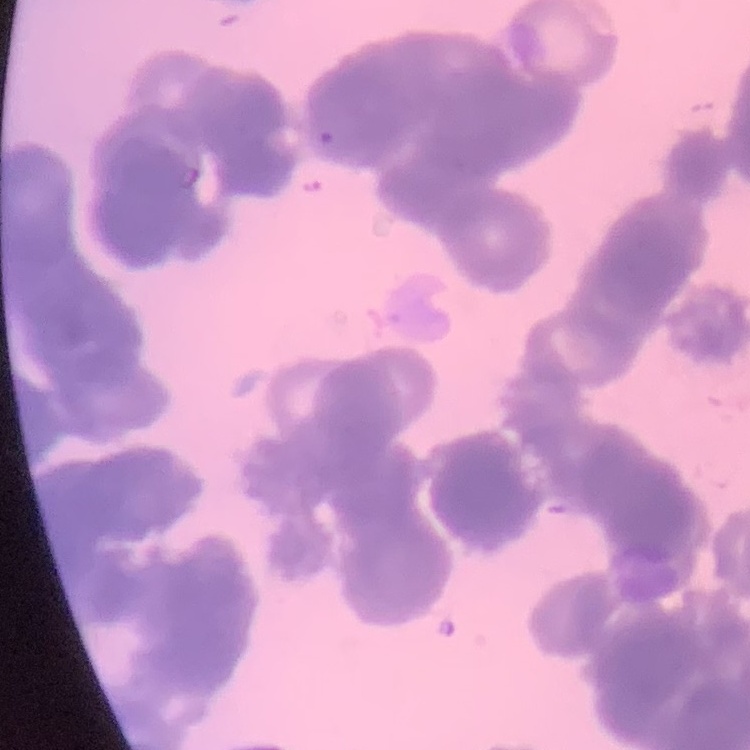
The red blood cells exhibit rouleaux formation. Stained with either Field's or Giemsa. Thin blood film. One tile cut from a larger photomicrograph.